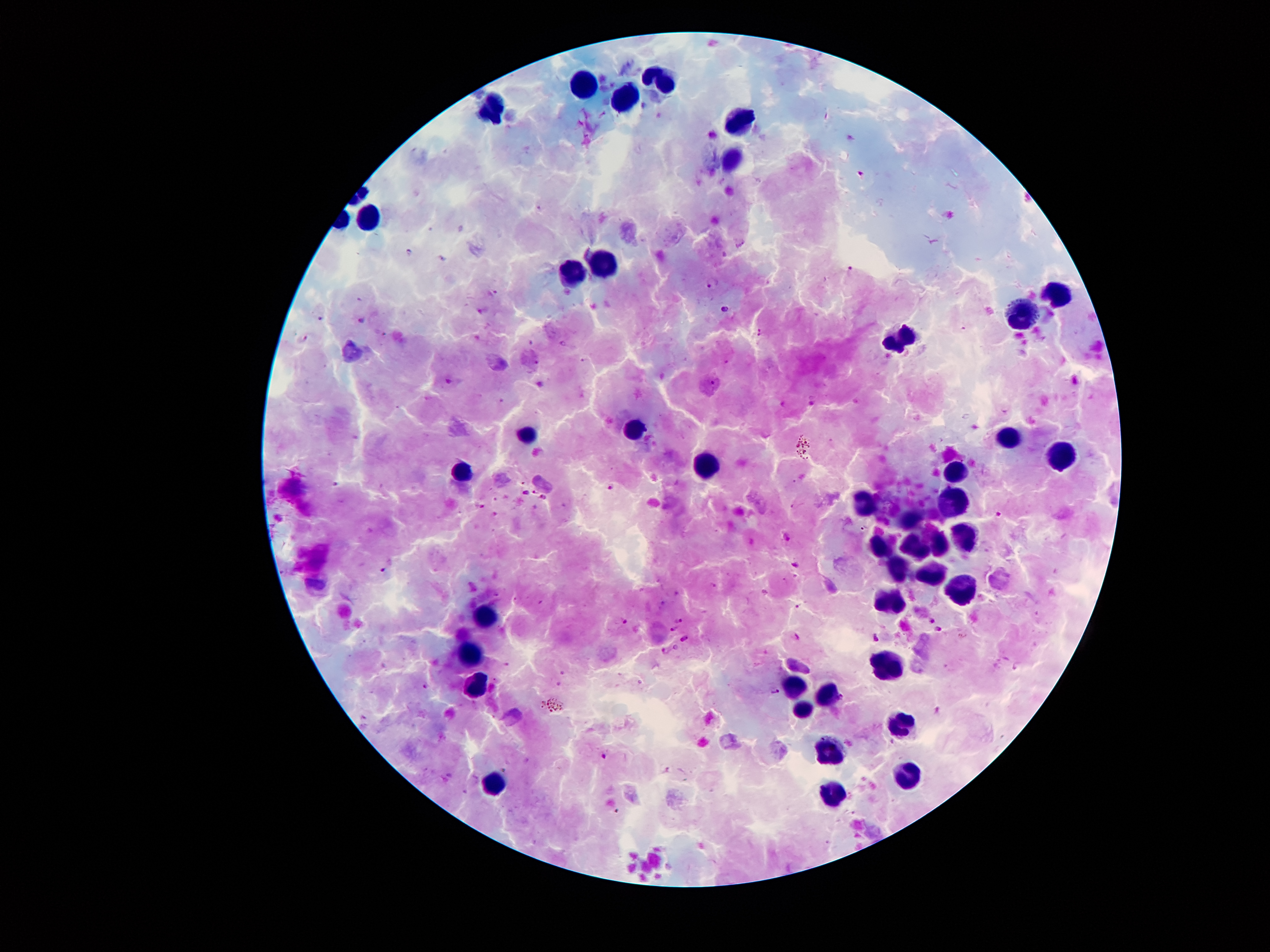

Approximate centers as (x, y) in pixels. Plasmodium parasite locations: (860, 172), (409, 251), (848, 270), (714, 283), (495, 293), (725, 309), (321, 320), (362, 320), (761, 332), (726, 362), (712, 383), (611, 487), (536, 491), (525, 493), (544, 498), (1001, 515), (381, 569), (680, 618), (932, 620), (625, 623), (672, 628), (939, 629), (798, 637), (875, 637), (684, 640), (675, 647), (666, 651), (425, 686), (775, 691), (605, 757), (505, 770). Leukocyte locations: (662, 76), (577, 87), (621, 97), (496, 109), (739, 116), (728, 156), (366, 209), (605, 261), (572, 270), (1059, 296), (1022, 318), (900, 335), (635, 428), (529, 434), (1012, 436), (1061, 456), (706, 465), (956, 470), (464, 473), (954, 497), (859, 499), (909, 521), (959, 534), (876, 545), (938, 545), (913, 548), (896, 565), (929, 574), (885, 592), (961, 596), (486, 616), (471, 654), (886, 666), (475, 683), (792, 690), (826, 690), (800, 710), (906, 720), (830, 750), (904, 771), (494, 784), (832, 792). Thick blood smear. Giemsa stain. 100x magnification. Single field of view. Photographed through the microscope eyepiece with a smartphone camera. Patient malaria status: positive for Plasmodium falciparum. Image is 1270×952 pixels.